Point out each leukocyte.
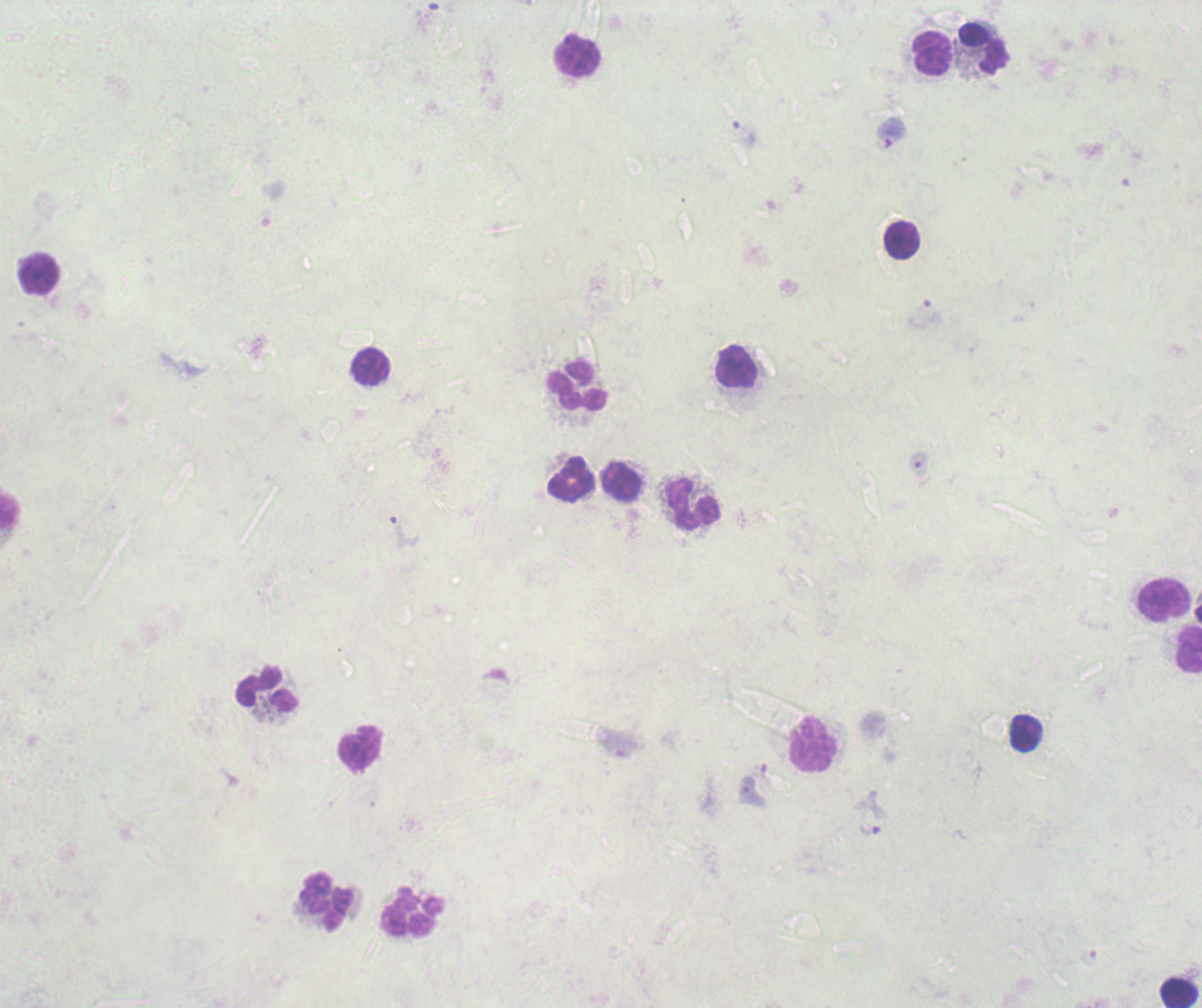
Approximate object centers, in pixels from the top-left corner.
Leukocytes: (x=983, y=48), (x=932, y=54), (x=578, y=58), (x=902, y=240), (x=38, y=274), (x=737, y=367), (x=370, y=368), (x=578, y=385), (x=573, y=480), (x=621, y=482), (x=694, y=504), (x=10, y=510), (x=1166, y=600), (x=1189, y=649), (x=266, y=690), (x=1026, y=733), (x=813, y=745), (x=359, y=748), (x=326, y=902), (x=412, y=914), (x=1179, y=994).

Approximate object centers, in pixels from the top-left corner. Trophozoite locations: (x=891, y=132), (x=872, y=813). Result: positive for Plasmodium parasites. 100x magnification. Thick blood smear. Background quality: poor. Image is 1202×1008 pixels. Previously used in an actual diagnosis. One field from this slide. Romanowsky stain.